State the preparation type.
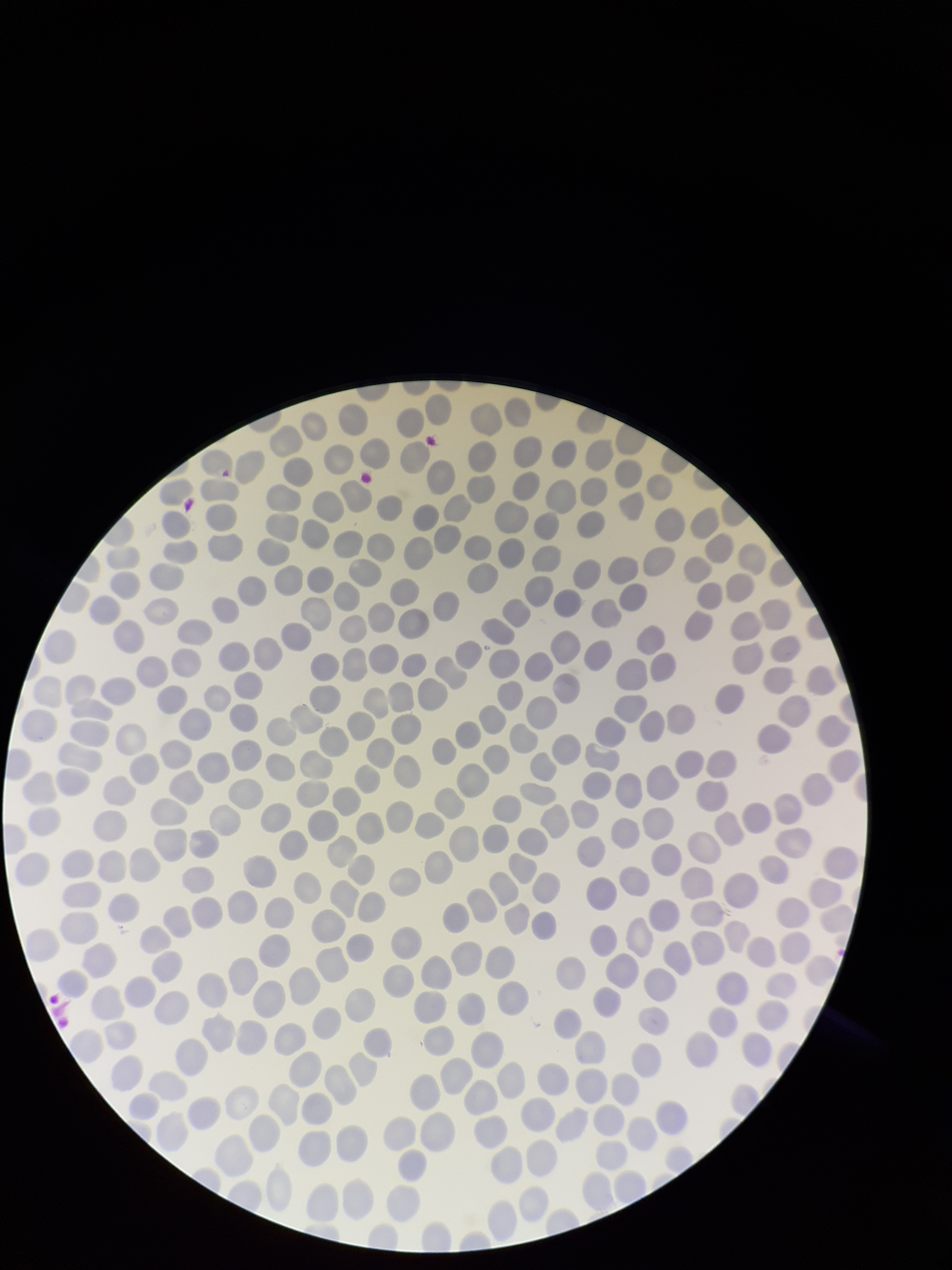

It is a thin blood smear.

parasitized red blood cells = none seen
stain = Giemsa
field of view = single
parasitized red blood cell count = 0
image size = 952×1270 pixels
patient malaria status = positive
species reported for this patient = Plasmodium falciparum
red blood cell count = 301
capture = smartphone photograph through the microscope eyepiece